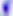

{
  "identification": "Toxoplasma gondii",
  "magnification": "400x",
  "modality": "photomicrograph"
}